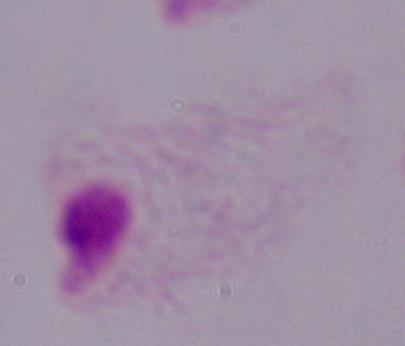
Micrograph. Captured at 1000x magnification. A trichomonad is seen.